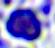

A leukocyte is seen. 400x magnification. Photomicrograph.